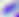

Summary:
  - Magnification: 400x
  - Modality: photomicrograph
  - Identification: Toxoplasma gondii